Give the extent of all white blood cells.
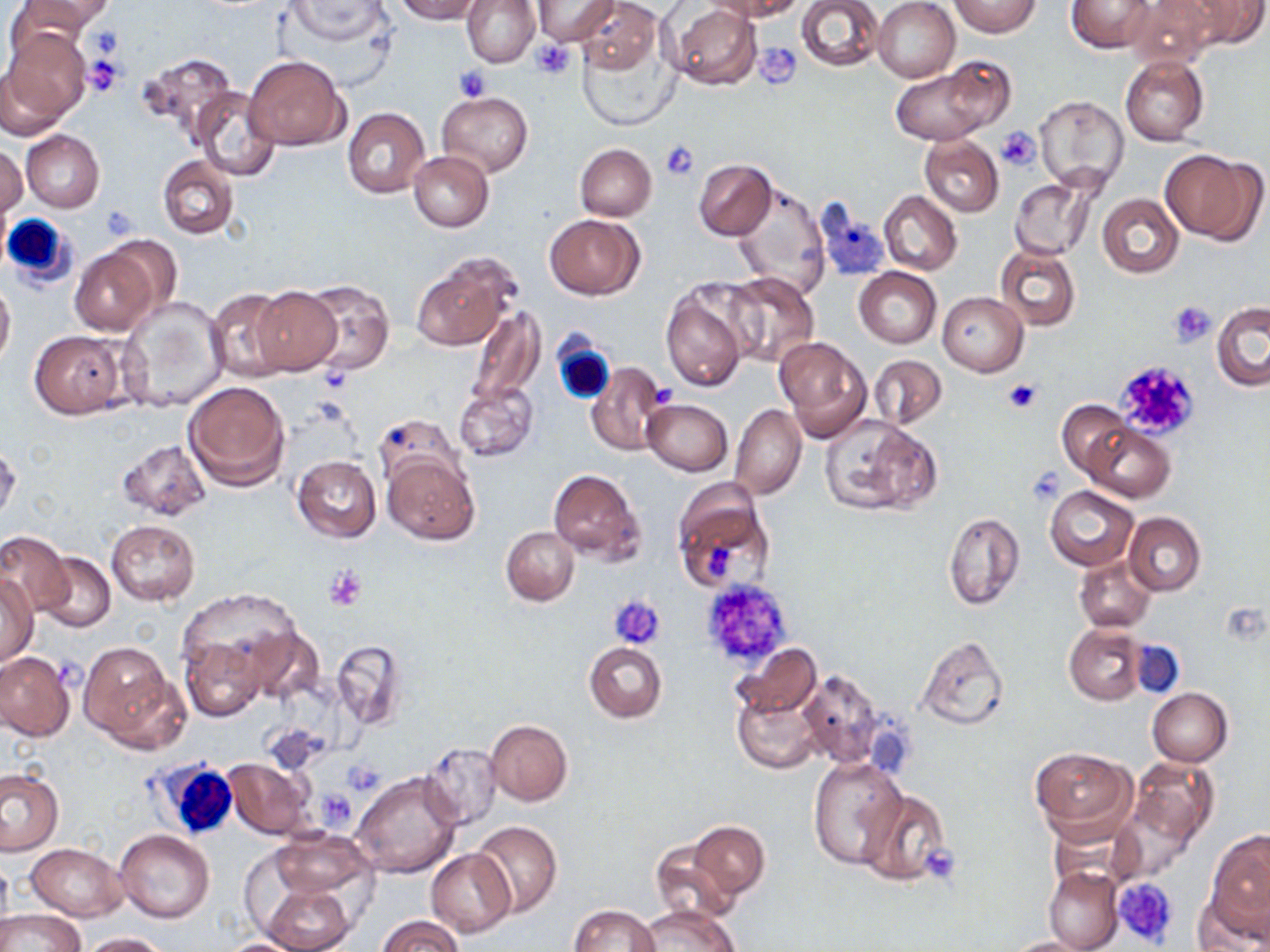
Approximate bounding boxes as named x1/y1/x2/y2 corners in pixels.
White blood cells: (x1=0, y1=213, x2=82, y2=288), (x1=552, y1=338, x2=615, y2=405), (x1=146, y1=758, x2=241, y2=840).

{
  "slide_level_diagnosis": "no evidence of blood parasites",
  "uninfected_red_blood_cell_locations": "approximate bounding boxes as named x1/y1/x2/y2 corners in pixels: (x1=10, y1=0, x2=113, y2=44), (x1=282, y1=0, x2=391, y2=46), (x1=392, y1=0, x2=484, y2=23), (x1=463, y1=0, x2=540, y2=67), (x1=532, y1=0, x2=619, y2=44), (x1=576, y1=0, x2=661, y2=79), (x1=709, y1=0, x2=805, y2=20), (x1=796, y1=0, x2=884, y2=72), (x1=873, y1=0, x2=960, y2=83), (x1=951, y1=0, x2=1040, y2=36), (x1=1067, y1=0, x2=1156, y2=54), (x1=1126, y1=0, x2=1218, y2=69), (x1=1183, y1=0, x2=1268, y2=49), (x1=666, y1=4, x2=762, y2=90), (x1=574, y1=24, x2=682, y2=133), (x1=2, y1=29, x2=89, y2=131), (x1=137, y1=53, x2=237, y2=140), (x1=244, y1=54, x2=347, y2=151), (x1=1119, y1=55, x2=1209, y2=146), (x1=887, y1=62, x2=1004, y2=148), (x1=193, y1=89, x2=281, y2=182), (x1=437, y1=91, x2=533, y2=176), (x1=1035, y1=96, x2=1129, y2=193), (x1=342, y1=108, x2=429, y2=198), (x1=20, y1=130, x2=104, y2=213), (x1=919, y1=135, x2=1003, y2=217), (x1=575, y1=144, x2=656, y2=221), (x1=0, y1=145, x2=26, y2=221), (x1=1162, y1=147, x2=1262, y2=244), (x1=408, y1=152, x2=493, y2=233), (x1=158, y1=156, x2=239, y2=239), (x1=694, y1=159, x2=777, y2=241), (x1=1009, y1=176, x2=1100, y2=261), (x1=731, y1=186, x2=831, y2=299), (x1=870, y1=189, x2=951, y2=348), (x1=879, y1=191, x2=962, y2=275), (x1=1098, y1=193, x2=1183, y2=277), (x1=545, y1=214, x2=644, y2=299), (x1=68, y1=244, x2=162, y2=335), (x1=995, y1=244, x2=1082, y2=331), (x1=410, y1=251, x2=520, y2=352), (x1=854, y1=268, x2=942, y2=348), (x1=720, y1=271, x2=819, y2=368), (x1=0, y1=277, x2=15, y2=370), (x1=300, y1=279, x2=394, y2=375), (x1=251, y1=287, x2=341, y2=373), (x1=206, y1=289, x2=291, y2=383), (x1=660, y1=289, x2=748, y2=392), (x1=938, y1=292, x2=1027, y2=375), (x1=116, y1=297, x2=230, y2=414), (x1=1211, y1=301, x2=1270, y2=392), (x1=465, y1=306, x2=544, y2=409), (x1=28, y1=330, x2=131, y2=419), (x1=773, y1=334, x2=869, y2=436), (x1=867, y1=354, x2=947, y2=431), (x1=585, y1=361, x2=670, y2=457), (x1=184, y1=381, x2=289, y2=491), (x1=453, y1=381, x2=538, y2=462), (x1=642, y1=399, x2=733, y2=475), (x1=1057, y1=400, x2=1132, y2=478), (x1=730, y1=403, x2=806, y2=500), (x1=373, y1=414, x2=463, y2=489), (x1=820, y1=414, x2=941, y2=517), (x1=1082, y1=423, x2=1174, y2=502), (x1=118, y1=439, x2=213, y2=522), (x1=0, y1=443, x2=20, y2=524), (x1=381, y1=451, x2=480, y2=545), (x1=292, y1=455, x2=382, y2=541), (x1=548, y1=468, x2=644, y2=562), (x1=671, y1=480, x2=774, y2=595), (x1=1044, y1=486, x2=1138, y2=570), (x1=943, y1=510, x2=1025, y2=611), (x1=1123, y1=512, x2=1206, y2=596), (x1=105, y1=520, x2=201, y2=604), (x1=502, y1=527, x2=578, y2=605), (x1=0, y1=533, x2=68, y2=616), (x1=36, y1=552, x2=115, y2=633), (x1=1074, y1=555, x2=1156, y2=633), (x1=0, y1=572, x2=38, y2=666), (x1=175, y1=603, x2=312, y2=711), (x1=1064, y1=625, x2=1145, y2=705), (x1=249, y1=629, x2=325, y2=704), (x1=915, y1=635, x2=1009, y2=730), (x1=182, y1=637, x2=266, y2=722), (x1=331, y1=639, x2=406, y2=729), (x1=584, y1=641, x2=667, y2=723), (x1=78, y1=642, x2=184, y2=750), (x1=732, y1=643, x2=821, y2=721), (x1=1, y1=653, x2=75, y2=741), (x1=795, y1=668, x2=887, y2=768), (x1=733, y1=686, x2=822, y2=773), (x1=1148, y1=688, x2=1233, y2=766), (x1=485, y1=719, x2=573, y2=806), (x1=420, y1=742, x2=502, y2=833), (x1=1029, y1=747, x2=1137, y2=843), (x1=1118, y1=755, x2=1219, y2=873), (x1=808, y1=756, x2=907, y2=870), (x1=223, y1=758, x2=314, y2=838), (x1=0, y1=768, x2=63, y2=855), (x1=351, y1=771, x2=462, y2=880), (x1=856, y1=788, x2=951, y2=887), (x1=686, y1=820, x2=771, y2=901), (x1=470, y1=821, x2=562, y2=918), (x1=114, y1=830, x2=215, y2=924), (x1=265, y1=830, x2=377, y2=905), (x1=1205, y1=830, x2=1270, y2=936), (x1=649, y1=840, x2=743, y2=923), (x1=27, y1=843, x2=128, y2=921), (x1=427, y1=849, x2=515, y2=936), (x1=0, y1=855, x2=12, y2=938), (x1=1044, y1=866, x2=1124, y2=952), (x1=261, y1=882, x2=354, y2=952), (x1=1195, y1=884, x2=1269, y2=952), (x1=567, y1=904, x2=661, y2=952), (x1=636, y1=905, x2=739, y2=952), (x1=0, y1=908, x2=83, y2=952), (x1=377, y1=915, x2=463, y2=952), (x1=75, y1=932, x2=171, y2=951), (x1=1001, y1=936, x2=1100, y2=952), (x1=214, y1=937, x2=313, y2=951)",
  "stain": "May-Grünwald-Giemsa",
  "image_size": "1270×952 pixels",
  "magnification": "1000x",
  "modality": "optical microscopy",
  "field_of_view": "single",
  "preparation": "thin blood film",
  "platelet_locations": "approximate bounding boxes as named x1/y1/x2/y2 corners in pixels: (x1=530, y1=40, x2=578, y2=79), (x1=754, y1=41, x2=799, y2=85), (x1=82, y1=56, x2=127, y2=97), (x1=453, y1=64, x2=493, y2=100), (x1=997, y1=128, x2=1039, y2=172), (x1=660, y1=140, x2=699, y2=181), (x1=99, y1=205, x2=138, y2=241), (x1=1168, y1=300, x2=1216, y2=347), (x1=1112, y1=360, x2=1200, y2=442), (x1=1003, y1=378, x2=1041, y2=414), (x1=1024, y1=468, x2=1066, y2=501), (x1=325, y1=565, x2=367, y2=611), (x1=699, y1=579, x2=794, y2=669), (x1=609, y1=595, x2=666, y2=650), (x1=343, y1=761, x2=385, y2=796), (x1=315, y1=789, x2=358, y2=831), (x1=923, y1=847, x2=964, y2=883), (x1=1112, y1=876, x2=1181, y2=949)"
}